State which cell type is depicted.
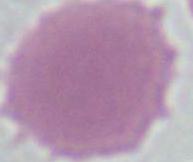
An erythrocyte.

Summary:
  - Modality: photomicrograph
  - Magnification: 1000x